Classify this cell by malaria status.
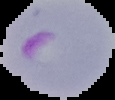
It is parasitized.

Image is 115×100 pixels. From a thin blood smear. Cell region segmented out of the field of view; the surrounding area is masked to black.